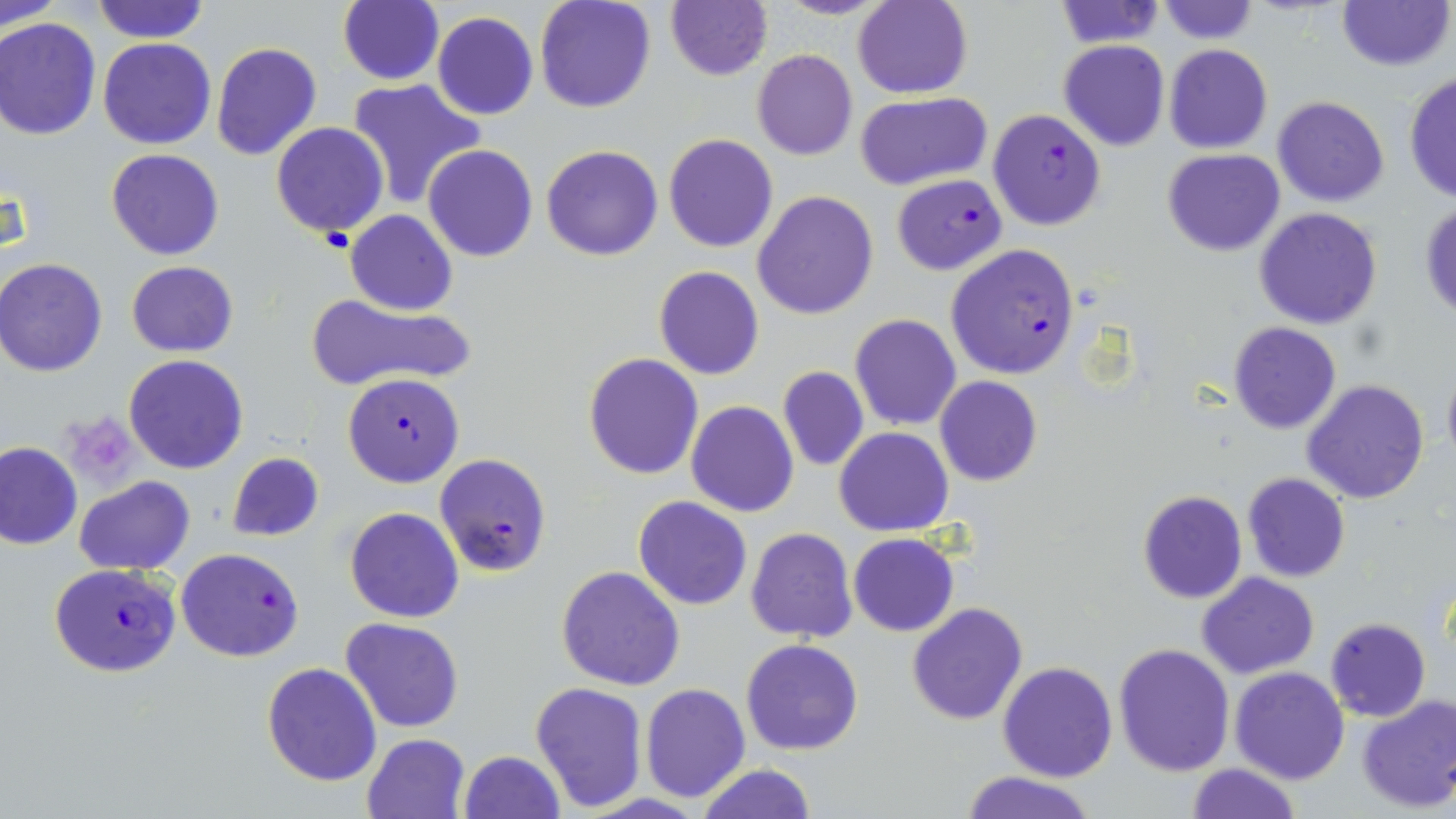

Summary:
  - Coordinate format: approximate bounding boxes as (x1, y1, x2, y2) in pixels
  - Plasmodium falciparum-infected red blood cell locations: (988, 108, 1107, 230), (893, 175, 1007, 275), (946, 243, 1079, 379), (342, 372, 466, 487), (435, 454, 553, 577), (176, 547, 304, 662), (49, 563, 181, 677)
  - Platelet locations: (323, 226, 353, 254), (74, 422, 138, 485)
  - Uninfected red blood cell locations: (0, 0, 62, 30), (90, 0, 211, 45), (337, 0, 444, 85), (534, 0, 657, 113), (665, 0, 773, 81), (771, 0, 896, 20), (854, 0, 971, 99), (1051, 0, 1165, 49), (1157, 0, 1258, 45), (1334, 0, 1453, 73), (432, 11, 539, 121), (0, 19, 101, 140), (97, 37, 217, 147), (1057, 40, 1171, 152), (210, 42, 322, 162), (1163, 44, 1273, 155), (752, 49, 857, 159), (1402, 70, 1455, 201), (345, 79, 487, 211), (855, 93, 989, 190), (1272, 95, 1392, 206), (271, 121, 389, 239), (663, 134, 779, 254), (541, 144, 664, 261), (423, 145, 538, 263), (106, 148, 225, 260), (1162, 148, 1287, 257), (753, 190, 877, 321), (1420, 201, 1456, 320), (1254, 208, 1383, 330), (341, 209, 460, 315), (0, 257, 108, 377), (126, 261, 239, 357), (654, 266, 765, 380), (304, 297, 475, 393), (850, 313, 962, 432), (1229, 322, 1341, 434), (583, 353, 703, 479), (124, 354, 249, 474), (1441, 361, 1456, 473), (777, 365, 869, 472), (934, 376, 1041, 486), (1301, 378, 1431, 503), (686, 402, 798, 517), (833, 427, 954, 537), (0, 441, 83, 550), (226, 451, 324, 543), (1241, 473, 1351, 583), (74, 475, 194, 575), (1136, 490, 1247, 604), (632, 495, 753, 611), (345, 507, 463, 623), (747, 528, 859, 643), (848, 532, 959, 637), (557, 566, 686, 690), (1196, 572, 1319, 680), (907, 602, 1028, 726), (1325, 617, 1432, 723), (340, 618, 464, 733), (740, 639, 865, 755), (1112, 642, 1235, 777), (997, 661, 1118, 782), (261, 663, 382, 786), (1229, 667, 1348, 785), (530, 681, 648, 811), (640, 682, 751, 802), (1355, 693, 1456, 811), (362, 732, 470, 818), (459, 750, 564, 819), (1186, 762, 1300, 818), (696, 764, 816, 819), (961, 771, 1096, 819)
  - Slide-level diagnosis: Plasmodium falciparum
  - Stain: May-Grünwald-Giemsa
  - Field of view: one of a larger specimen
  - Image size: 1456×819 pixels
  - Magnification: 1000x
  - Modality: light microscopy
  - Preparation: thin blood film